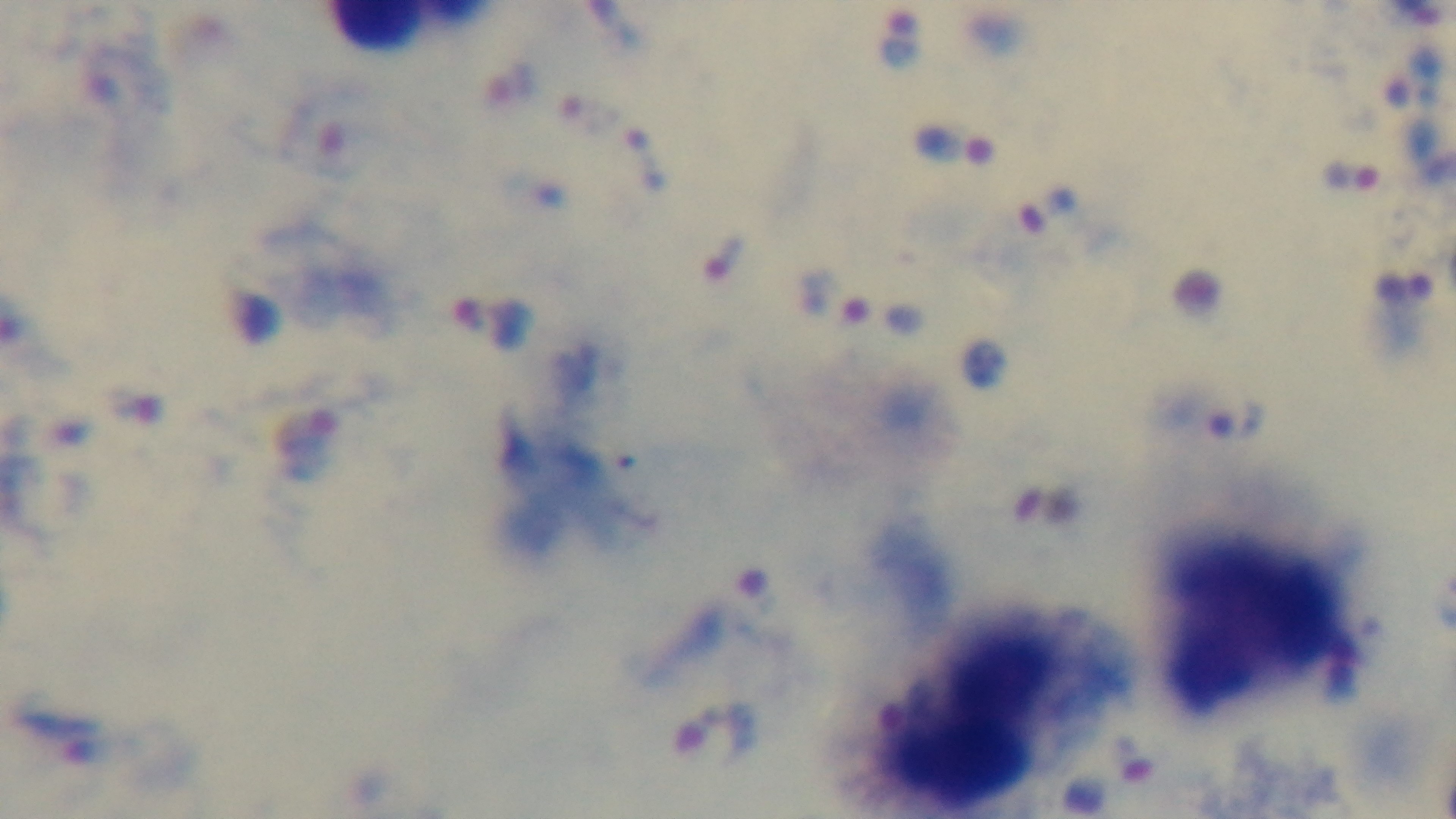
Summary:
  - Modality: light microscopy
  - Objective: 100x oil immersion
  - Capture: mounted 4K digital camera
  - Stain: Giemsa
  - Preparation: thick blood film
  - Malaria status: positive
  - Field of view: one from the slide